State the blood parasite species.
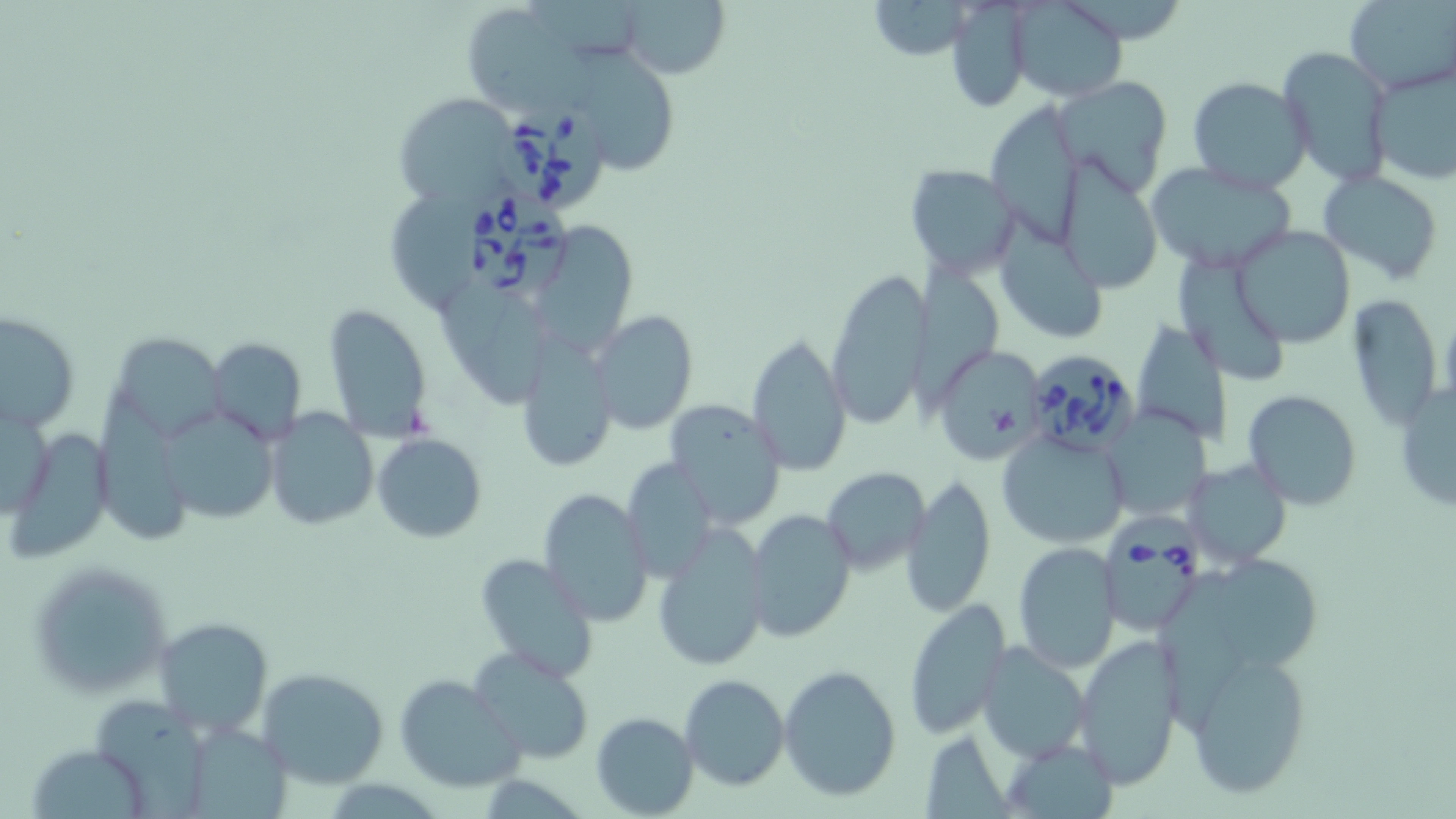

Babesia divergens.

Summary:
  - Coordinate format: approximate bounding boxes as (x1,y1)-(x2,y2) corner pairs in pixels
  - Babesia divergens-infected red blood cell locations: (496,98)-(614,215), (466,189)-(568,302), (1035,341)-(1139,451), (1098,506)-(1201,636)
  - Uninfected red blood cell locations: (618,0)-(728,78), (865,0)-(980,61), (1009,1)-(1129,101), (1346,2)-(1454,91), (945,4)-(1037,112), (462,7)-(588,106), (581,41)-(686,177), (1279,45)-(1392,189), (1371,65)-(1456,189), (1056,75)-(1174,196), (1188,75)-(1311,194), (391,91)-(526,211), (988,98)-(1093,245), (1066,155)-(1158,296), (904,163)-(1021,275), (1146,164)-(1298,272), (1319,171)-(1446,285), (388,184)-(485,312), (997,211)-(1107,338), (542,222)-(647,351), (1232,224)-(1356,348), (1180,249)-(1286,378), (907,260)-(1004,411), (824,270)-(932,430), (446,287)-(550,403), (1344,289)-(1444,431), (323,303)-(434,444), (2,310)-(79,435), (590,311)-(697,433), (1133,314)-(1232,450), (119,331)-(237,439), (746,332)-(852,473), (206,337)-(307,443), (517,338)-(616,473), (931,345)-(1050,464), (1393,376)-(1455,515), (95,381)-(198,550), (1243,390)-(1362,510), (1,395)-(52,525), (663,401)-(787,528), (264,407)-(378,531), (1101,407)-(1209,520), (159,409)-(282,530), (8,427)-(112,558), (997,431)-(1131,549), (372,433)-(487,543), (623,456)-(719,580), (1185,459)-(1291,568), (823,468)-(931,574), (902,472)-(998,620), (538,488)-(653,628), (741,508)-(857,644), (651,527)-(770,671), (1012,541)-(1120,671), (1228,551)-(1322,677), (476,554)-(600,683), (29,559)-(171,697), (1163,578)-(1251,739), (903,600)-(1010,738), (151,617)-(272,736), (1072,633)-(1186,790), (977,639)-(1092,762), (1180,645)-(1316,798), (471,650)-(596,765), (779,665)-(903,801), (254,668)-(389,788), (393,672)-(525,794), (680,673)-(789,791), (99,696)-(213,819), (590,711)-(698,818), (186,723)-(300,819), (918,730)-(1012,816), (1005,739)-(1121,817), (28,743)-(152,819)
  - Stain: May-Grünwald-Giemsa
  - Modality: optical microscopy
  - Preparation: thin blood smear
  - Image size: 1456×819 pixels
  - Magnification: 1000x
  - Field of view: one of a larger specimen